Comment on the morphology of the erythrocytes.
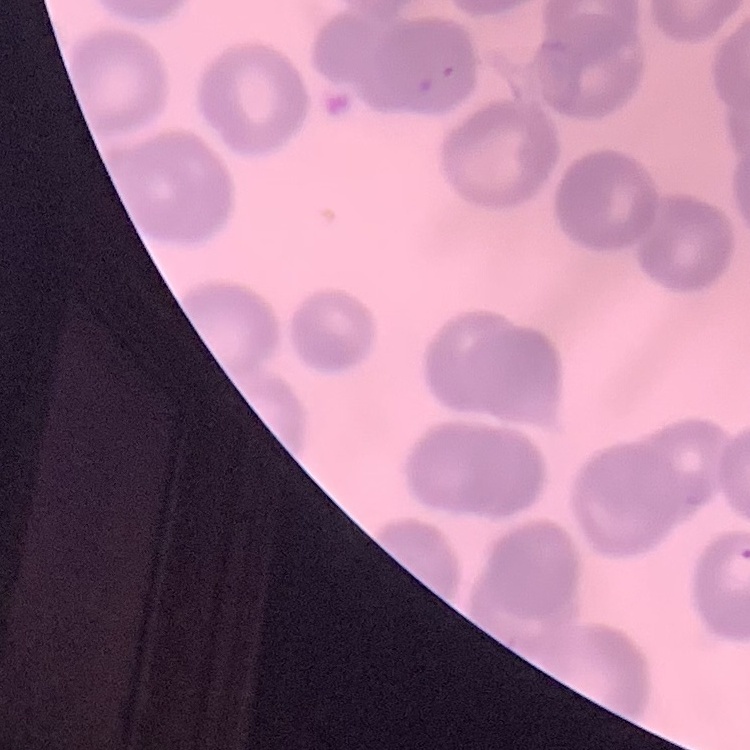

They show no rouleaux formation.

image type = one tile cut from a larger photomicrograph
stain = Field's or Giemsa
preparation = thin blood film